Outline platelets.
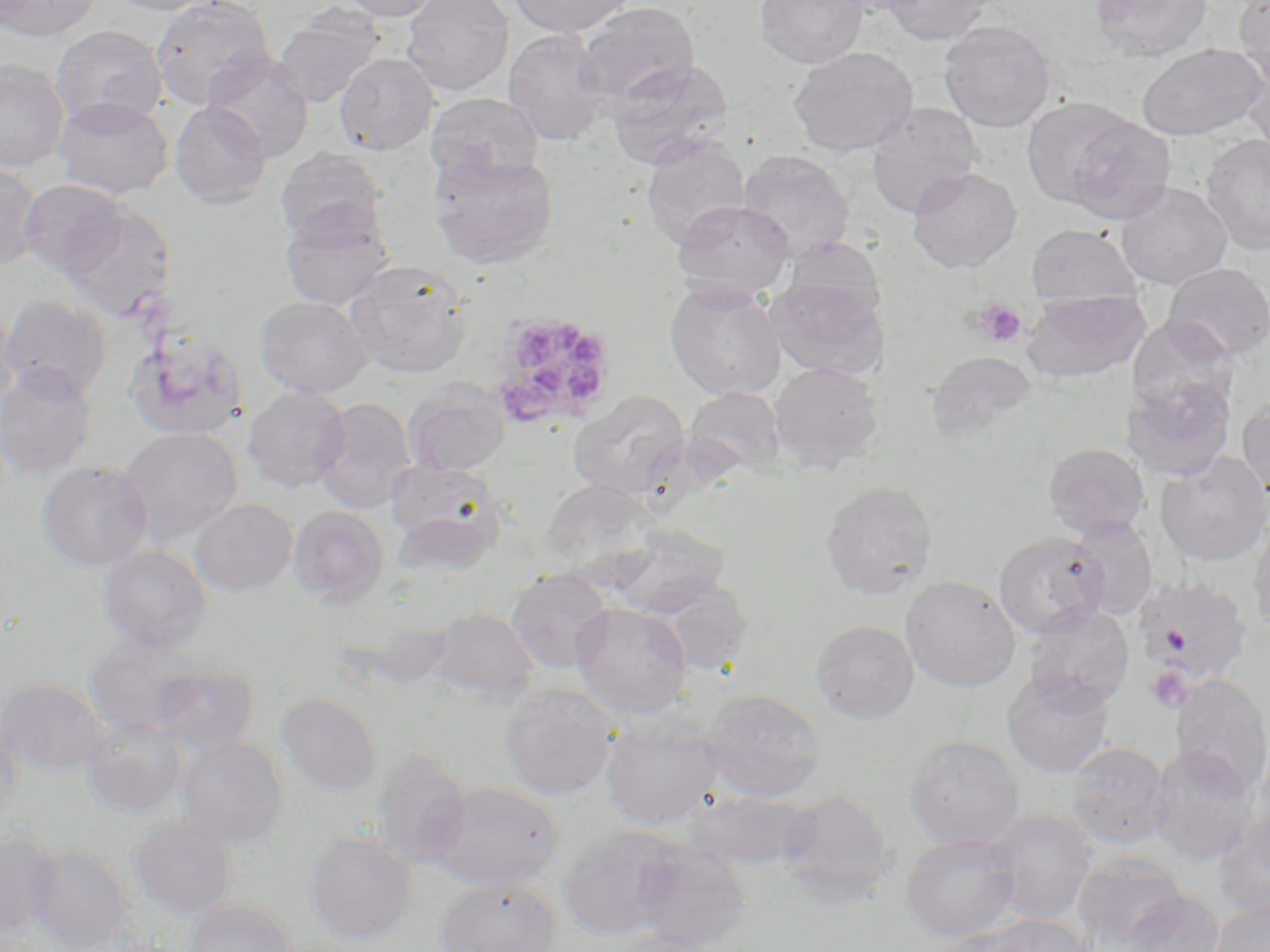
Approximate bounding boxes as [x1, y1, x2, y2] in pixels.
Platelets: [967, 297, 1027, 348], [483, 311, 619, 430], [1145, 666, 1193, 712].

{
  "slide_level_diagnosis": "Plasmodium ovale",
  "preparation": "thin blood smear",
  "image_size": "1270×952 pixels",
  "modality": "light microscopy",
  "uninfected_red_blood_cell_locations": "approximate bounding boxes as [x1, y1, x2, y2] in pixels: [0, 0, 101, 42], [103, 0, 220, 15], [150, 0, 275, 110], [339, 0, 446, 21], [402, 0, 514, 97], [508, 0, 634, 37], [754, 0, 869, 69], [883, 0, 994, 45], [1090, 0, 1213, 62], [1234, 0, 1270, 87], [576, 2, 701, 109], [272, 6, 384, 108], [939, 21, 1057, 132], [51, 25, 167, 129], [503, 30, 608, 146], [1137, 43, 1266, 141], [789, 45, 919, 156], [1240, 47, 1270, 156], [205, 50, 314, 161], [335, 52, 440, 155], [606, 57, 733, 168], [0, 59, 69, 173], [426, 92, 544, 184], [53, 96, 173, 199], [1020, 97, 1137, 208], [169, 102, 271, 210], [865, 103, 981, 219], [1062, 115, 1176, 225], [1201, 134, 1270, 254], [641, 136, 750, 249], [276, 148, 387, 246], [737, 150, 855, 261], [429, 151, 559, 270], [0, 159, 44, 273], [907, 167, 1023, 274], [19, 179, 128, 278], [1115, 181, 1232, 290], [60, 199, 177, 322], [671, 200, 795, 301], [279, 204, 394, 312], [1026, 223, 1142, 309], [346, 261, 472, 379], [1162, 263, 1270, 363], [768, 275, 891, 381], [664, 280, 786, 402], [1023, 290, 1150, 385], [1, 293, 111, 402], [255, 296, 372, 398], [0, 306, 20, 414], [125, 330, 248, 441], [926, 351, 1038, 443], [769, 362, 885, 473], [0, 363, 98, 482], [1126, 375, 1236, 482], [403, 380, 510, 476], [243, 386, 350, 493], [685, 386, 786, 478], [569, 390, 690, 499], [1237, 396, 1270, 500], [311, 398, 417, 513], [118, 427, 243, 546], [1043, 442, 1150, 538], [1154, 451, 1270, 566], [386, 460, 507, 565], [35, 461, 154, 573], [538, 479, 660, 570], [820, 480, 939, 600], [190, 499, 297, 597], [288, 506, 389, 609], [1067, 516, 1158, 620], [1247, 518, 1270, 637], [610, 524, 729, 617], [994, 531, 1109, 638], [96, 545, 212, 652], [506, 567, 614, 673], [901, 575, 1021, 692], [1133, 575, 1253, 686], [649, 578, 756, 677], [570, 602, 692, 720], [1024, 603, 1135, 711], [427, 608, 540, 701], [810, 619, 919, 724], [84, 635, 202, 736], [150, 658, 259, 755], [1002, 669, 1115, 778], [1169, 673, 1270, 798], [0, 678, 106, 777], [498, 685, 620, 801], [698, 689, 826, 803], [277, 692, 382, 796], [0, 707, 24, 822], [600, 713, 725, 830], [80, 715, 186, 818], [904, 734, 1025, 849], [174, 735, 289, 850], [1065, 741, 1172, 850], [1147, 746, 1261, 866], [370, 750, 473, 865], [425, 782, 566, 889], [775, 787, 896, 906], [682, 791, 816, 871], [983, 809, 1098, 923], [1213, 810, 1270, 918], [128, 819, 237, 919], [557, 827, 687, 941], [303, 829, 419, 944], [0, 831, 62, 942], [900, 833, 1022, 942], [626, 840, 752, 951], [24, 842, 135, 952], [1072, 853, 1188, 950], [432, 877, 562, 951], [1121, 890, 1225, 952], [183, 899, 296, 952], [1209, 899, 1270, 952], [969, 913, 1095, 952], [927, 928, 1038, 952], [602, 933, 725, 952]",
  "stain": "May-Grünwald-Giemsa",
  "magnification": "1000x",
  "field_of_view": "one of a larger specimen"
}